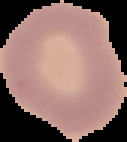
The area outside the segmented cell region is set to black. Image is 127×142 pixels. From a thin blood smear. Result: no Plasmodium parasites seen.